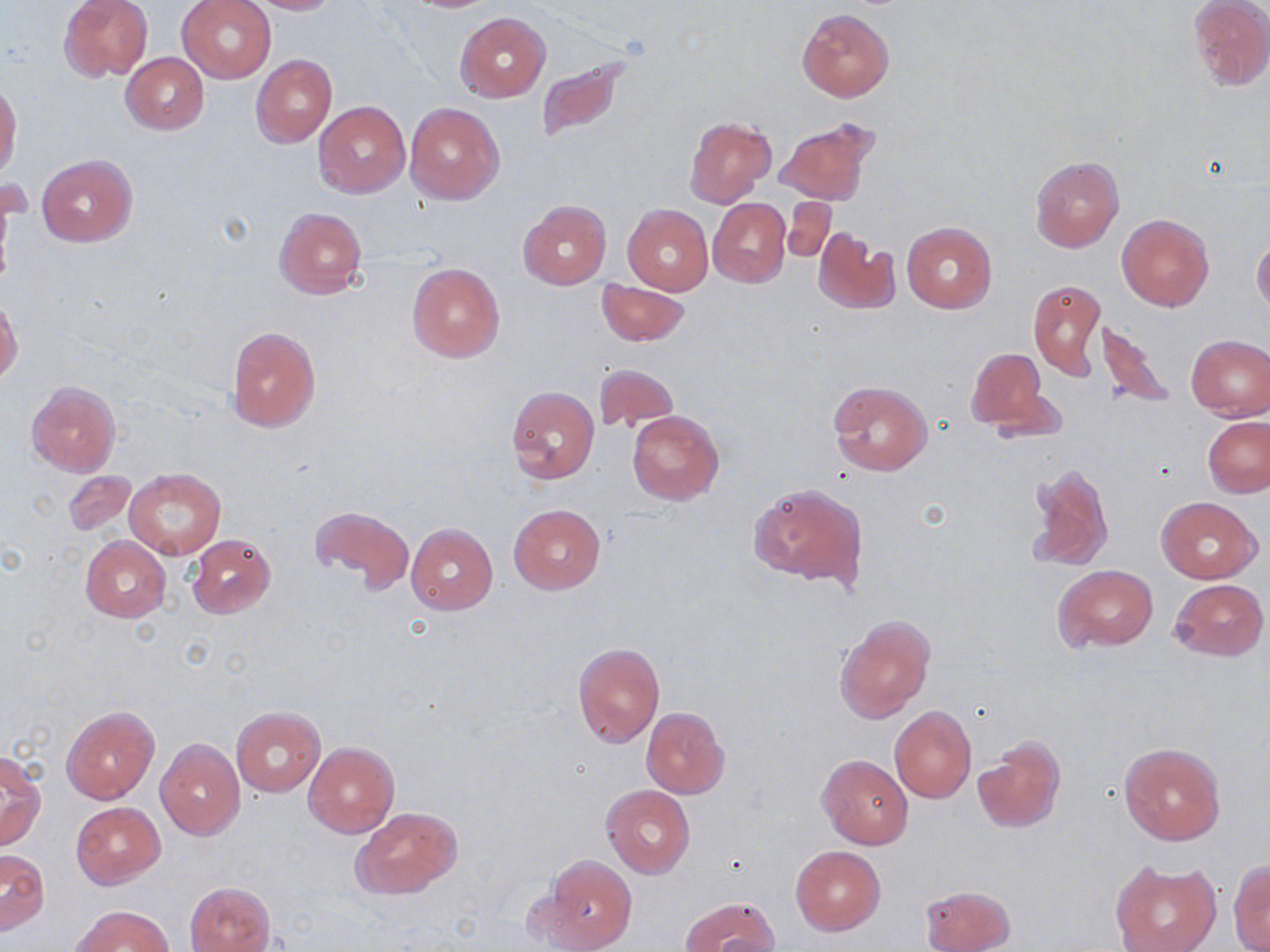

{
  "slide_level_diagnosis": "no evidence of blood parasites",
  "preparation": "thin blood film",
  "magnification": "1000x",
  "stain": "May-Grünwald-Giemsa",
  "uninfected_red_blood_cell_locations": "approximate bounding boxes as named x1/y1/x2/y2 corners in pixels: (x1=58, y1=0, x2=153, y2=82), (x1=178, y1=0, x2=276, y2=83), (x1=249, y1=0, x2=338, y2=14), (x1=399, y1=0, x2=504, y2=13), (x1=1188, y1=0, x2=1270, y2=90), (x1=796, y1=8, x2=894, y2=101), (x1=455, y1=12, x2=551, y2=102), (x1=121, y1=53, x2=208, y2=135), (x1=251, y1=53, x2=336, y2=148), (x1=534, y1=54, x2=637, y2=143), (x1=0, y1=84, x2=22, y2=181), (x1=314, y1=101, x2=410, y2=197), (x1=405, y1=102, x2=504, y2=203), (x1=684, y1=116, x2=776, y2=206), (x1=774, y1=118, x2=879, y2=206), (x1=37, y1=154, x2=137, y2=247), (x1=1030, y1=155, x2=1123, y2=252), (x1=782, y1=196, x2=838, y2=263), (x1=708, y1=198, x2=790, y2=287), (x1=518, y1=200, x2=612, y2=290), (x1=623, y1=205, x2=713, y2=295), (x1=274, y1=208, x2=367, y2=299), (x1=1117, y1=213, x2=1214, y2=311), (x1=901, y1=221, x2=997, y2=312), (x1=813, y1=229, x2=899, y2=316), (x1=1252, y1=235, x2=1270, y2=314), (x1=407, y1=262, x2=504, y2=362), (x1=596, y1=279, x2=688, y2=345), (x1=1027, y1=279, x2=1106, y2=379), (x1=1, y1=299, x2=22, y2=383), (x1=1092, y1=316, x2=1176, y2=409), (x1=225, y1=326, x2=321, y2=432), (x1=1185, y1=334, x2=1270, y2=420), (x1=965, y1=347, x2=1053, y2=433), (x1=594, y1=363, x2=677, y2=434), (x1=828, y1=380, x2=933, y2=476), (x1=26, y1=381, x2=120, y2=477), (x1=507, y1=387, x2=598, y2=485), (x1=627, y1=410, x2=724, y2=505), (x1=1203, y1=415, x2=1270, y2=497), (x1=1024, y1=461, x2=1114, y2=570), (x1=125, y1=468, x2=227, y2=560), (x1=61, y1=471, x2=136, y2=537), (x1=749, y1=482, x2=867, y2=588), (x1=1158, y1=497, x2=1262, y2=582), (x1=309, y1=504, x2=414, y2=592), (x1=509, y1=504, x2=605, y2=595), (x1=316, y1=514, x2=499, y2=602), (x1=406, y1=523, x2=498, y2=614), (x1=187, y1=534, x2=276, y2=619), (x1=80, y1=536, x2=170, y2=622), (x1=1052, y1=564, x2=1159, y2=651), (x1=1169, y1=578, x2=1269, y2=661), (x1=834, y1=613, x2=935, y2=724), (x1=572, y1=643, x2=664, y2=747), (x1=61, y1=706, x2=159, y2=803), (x1=231, y1=706, x2=326, y2=796), (x1=889, y1=706, x2=976, y2=803), (x1=641, y1=707, x2=731, y2=798), (x1=974, y1=735, x2=1065, y2=833), (x1=156, y1=738, x2=244, y2=840), (x1=1118, y1=741, x2=1226, y2=847), (x1=303, y1=742, x2=399, y2=837), (x1=1, y1=753, x2=46, y2=852), (x1=816, y1=753, x2=914, y2=850), (x1=601, y1=784, x2=695, y2=878), (x1=71, y1=802, x2=165, y2=888), (x1=351, y1=807, x2=462, y2=901), (x1=791, y1=845, x2=885, y2=935), (x1=0, y1=851, x2=48, y2=936), (x1=536, y1=854, x2=637, y2=952), (x1=1229, y1=860, x2=1270, y2=952), (x1=1110, y1=862, x2=1222, y2=952), (x1=185, y1=882, x2=275, y2=952), (x1=922, y1=884, x2=1014, y2=952), (x1=680, y1=895, x2=779, y2=952), (x1=73, y1=905, x2=173, y2=951)",
  "field_of_view": "single",
  "image_size": "1270×952 pixels",
  "modality": "optical microscopy"
}